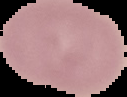

image type = cell region segmented out of the field of view; surrounding area masked to black
image size = 127×97 pixels
preparation = thin blood film
malaria status = uninfected